Report the malaria status of this cell.
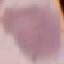

Uninfected.

Thin blood smear. Photographed with a smartphone camera at the microscope eyepiece. Cell patch, automatically extracted from a larger field of view and resized to 64 × 64 pixels. Giemsa stain.